State which parasite is depicted.
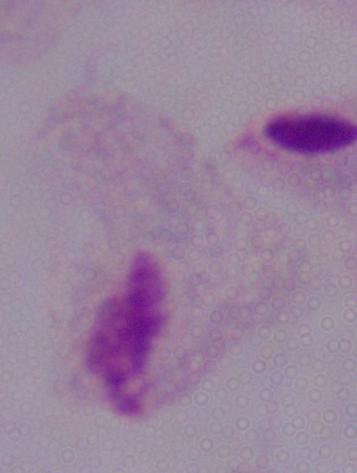
This is a trichomonad.

Photomicrograph. Captured at 1000x magnification.